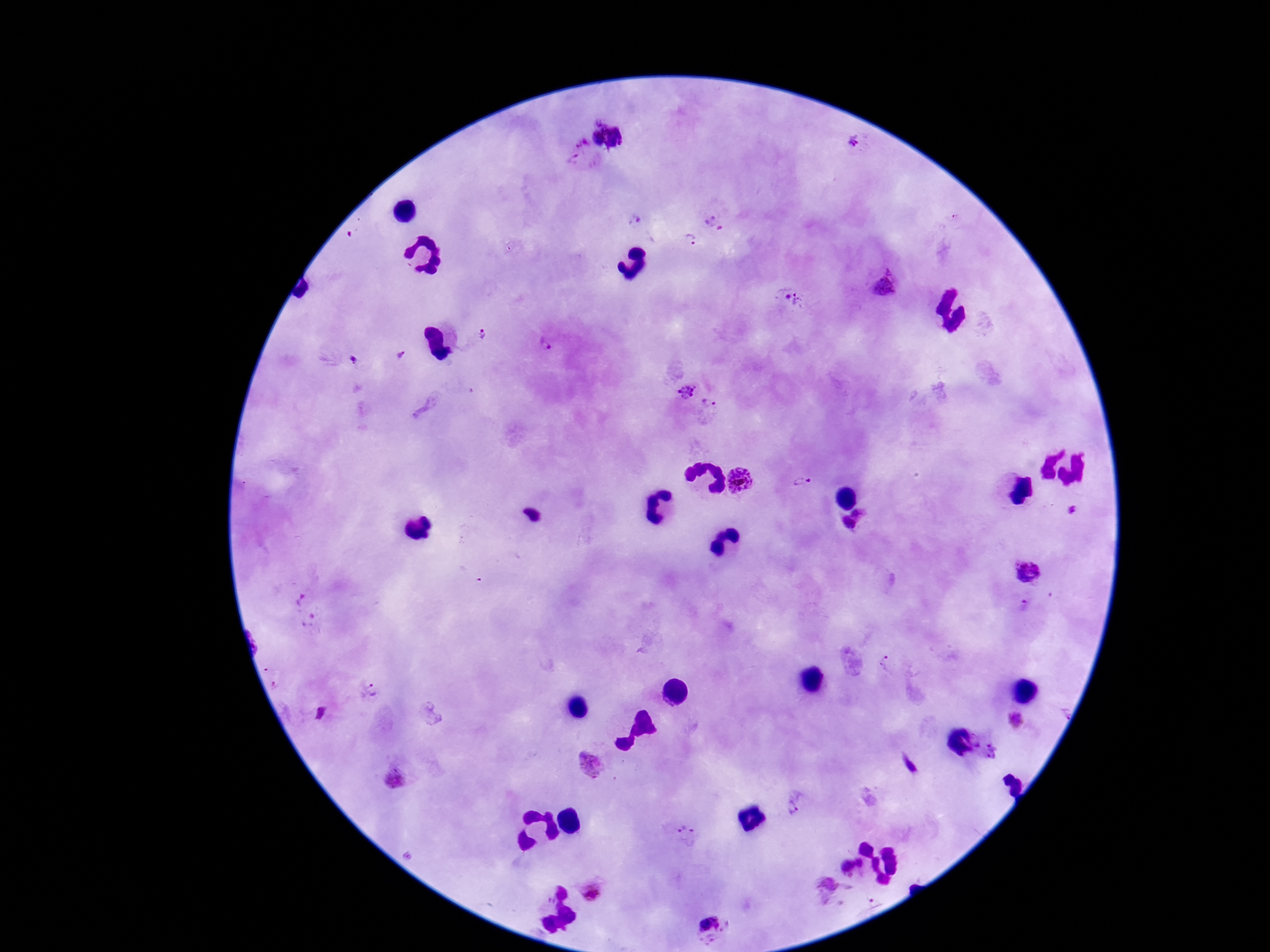

Approximate object centers, in pixels from the top-left corner. Plasmodium parasite locations: (x=582, y=141), (x=852, y=143), (x=573, y=162), (x=710, y=218), (x=638, y=221), (x=689, y=240), (x=885, y=285), (x=792, y=302), (x=483, y=335), (x=546, y=345), (x=400, y=356), (x=351, y=360), (x=684, y=393), (x=708, y=406), (x=740, y=483), (x=803, y=483), (x=1074, y=509), (x=857, y=512), (x=848, y=522), (x=1028, y=572), (x=297, y=598), (x=1027, y=606), (x=312, y=621), (x=887, y=666), (x=371, y=691), (x=1016, y=721), (x=591, y=764), (x=909, y=765), (x=397, y=778), (x=796, y=804), (x=685, y=831), (x=861, y=863), (x=845, y=868), (x=829, y=889), (x=593, y=891), (x=871, y=900), (x=710, y=924). Thick blood smear. Patient malaria status: positive. One field from this slide. Giemsa stain. Photographed through the microscope eyepiece with a smartphone camera. 100x magnification. Image is 1270×952 pixels.